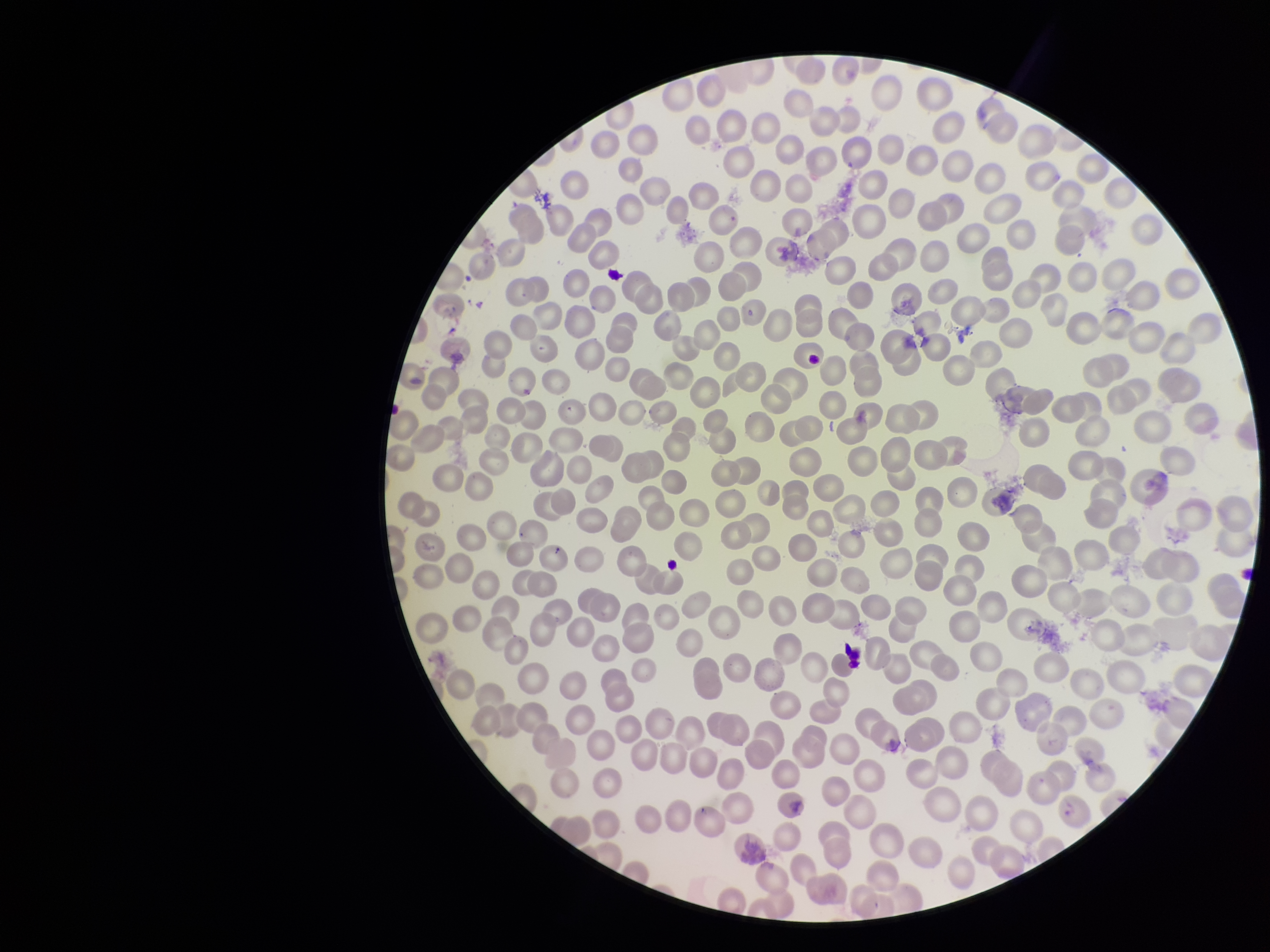

Red blood cell count: 326. Parasitized red blood cell count: 0. Image is 1270×952 pixels. Patient malaria status: infected. Species reported for this patient: Plasmodium falciparum. Photographed through the microscope eyepiece with a smartphone camera. Preparation: thin smear. Stained with Giemsa. Single field of view. Parasitized red blood cells: none identified.